Draw a bounding box around every Plasmodium parasite.
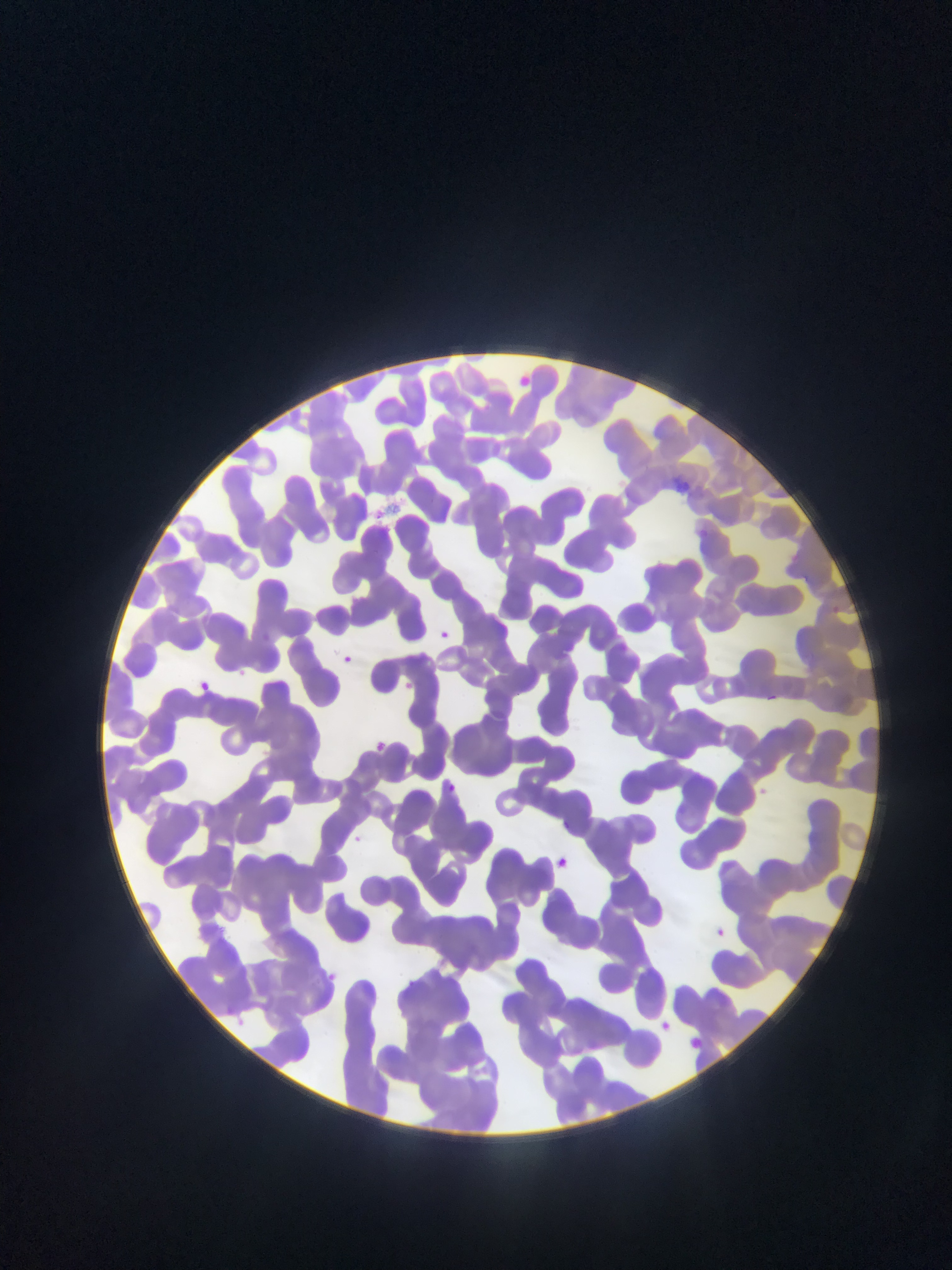

Approximate bounding boxes as left top right bottom in pixels.
Plasmodium parasites: 437 627 454 642; 336 651 355 670; 235 666 252 681; 194 678 213 696; 399 679 416 695; 762 690 779 706; 369 739 389 755; 440 779 460 797; 346 832 366 850; 548 854 574 875; 705 922 732 945; 320 968 342 988; 397 977 421 997; 220 1009 256 1039; 654 1015 675 1037; 680 1032 708 1057.

Image is 952×1270 pixels. One field of view. Thin blood film. Sample from Ghana. Photographed through a microscope with a mobile-phone camera.